Classify this cell by malaria status.
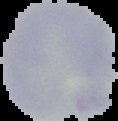
Uninfected.

Summary:
  - Preparation: thin blood film
  - Image type: segmented cell region on a black background
  - Image size: 118×121 pixels